Name the cell type shown.
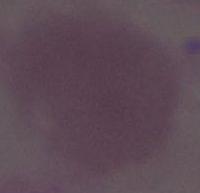
An erythrocyte.

Summary:
  - Magnification: 1000x
  - Modality: photomicrograph